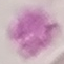
Summary:
  - Result: no malaria parasites detected
  - Preparation: thin blood smear
  - Capture: smartphone through the microscope eyepiece
  - Image type: cell patch, automatically extracted from a larger field of view and resized to 64 × 64 pixels
  - Stain: Giemsa